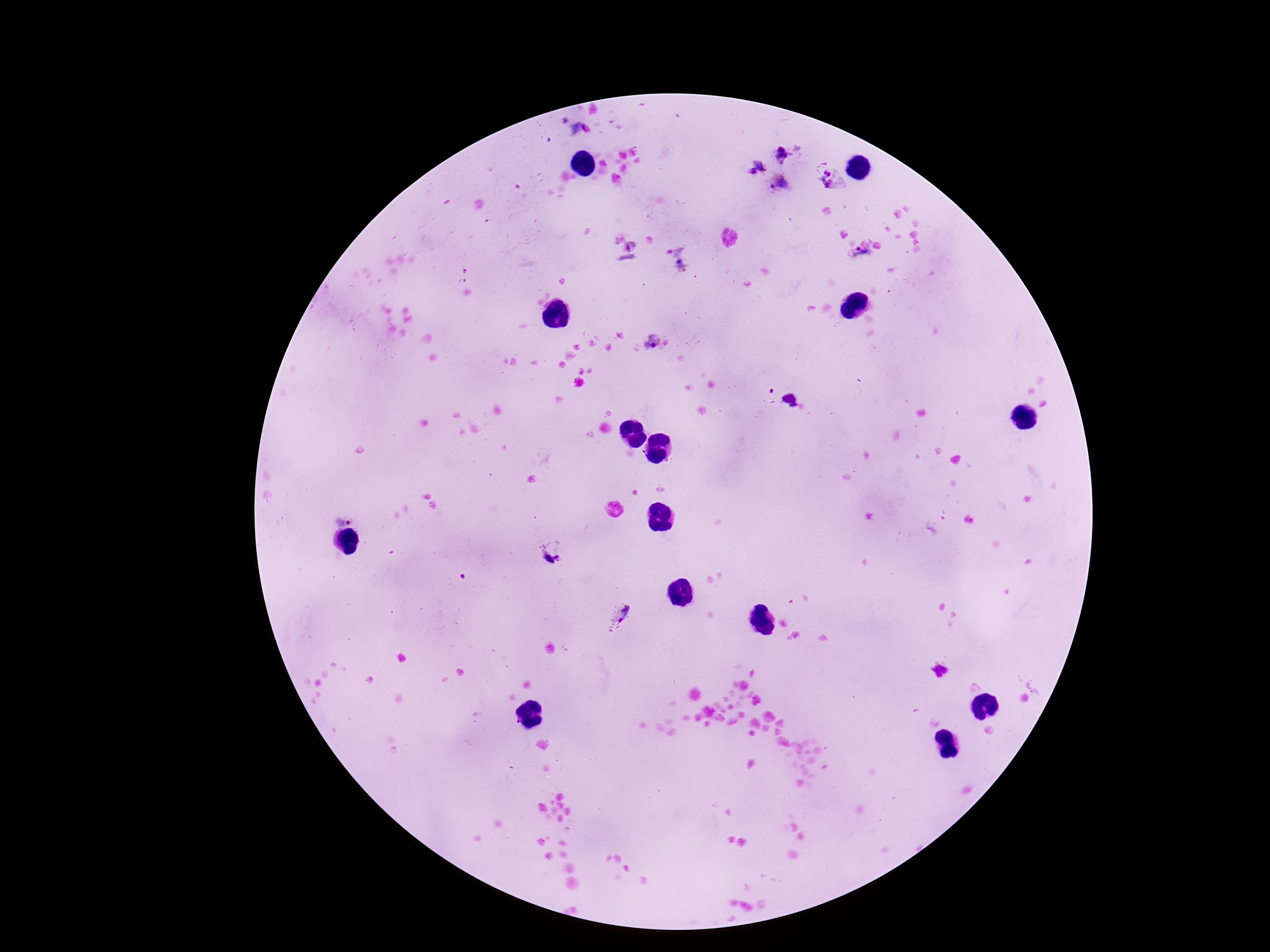
magnification: 100x
preparation: thick peripheral-blood smear
stain: Giemsa
capture: smartphone camera through the microscope eyepiece
image_size: 1270×952 pixels
plasmodium_parasite_locations: 'approximate centers as [x, y] in pixels: [653, 342], [344, 517], [552, 551], [621, 616]'
field_of_view: single
patient_malaria_status: infected